Report the malaria status of this cell.
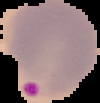
It is parasitized.

Image is 100×103 pixels. From a thin blood film. Segmented cell region on a black background.